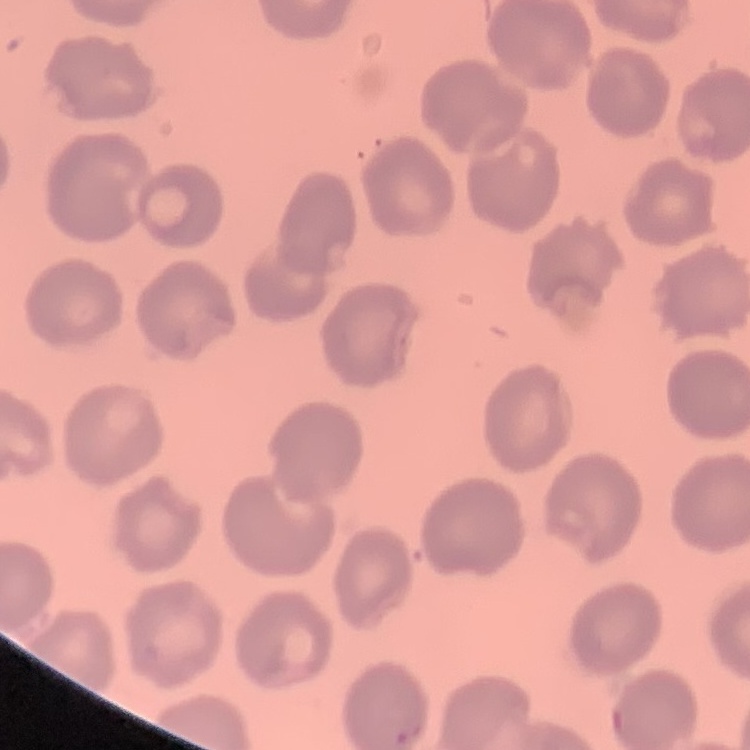
red blood cell morphology = no rouleaux formation
image type = square crop of a larger photomicrograph
preparation = thin blood film
stain = Field's or Giemsa